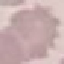

malaria status = uninfected
capture = smartphone camera at the microscope eyepiece
preparation = thin blood film
image type = automatically extracted cell patch, resized to 64 × 64 pixels
stain = Giemsa